Assess this cell for malaria.
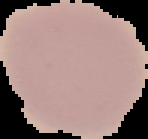

It is uninfected.

image type = cell region segmented out of the field of view; surrounding area masked to black
preparation = thin blood smear
image size = 148×139 pixels